Describe the morphology of the erythrocytes.
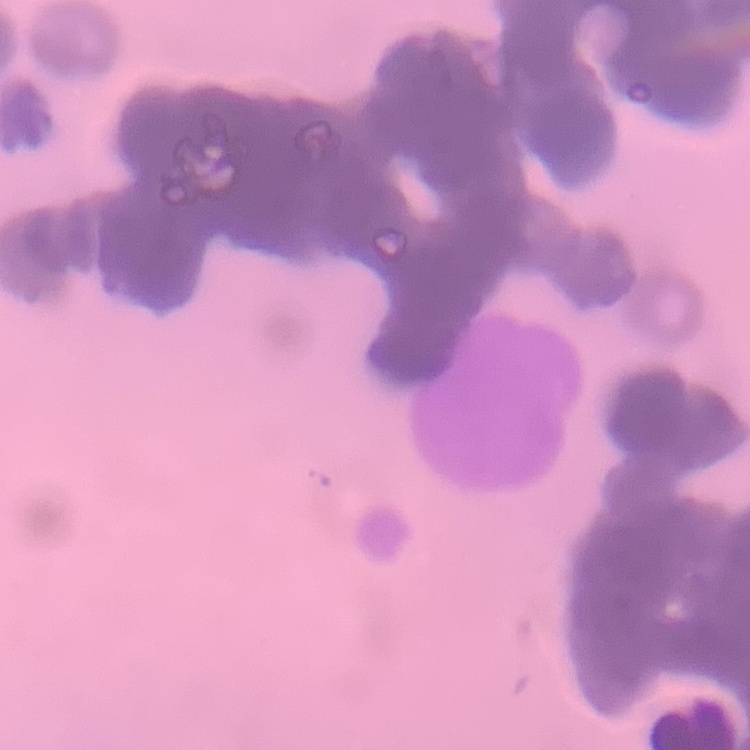
They show rouleaux formation.

Thin peripheral smear. Stained with either Field's or Giemsa. Square crop of a larger photomicrograph.